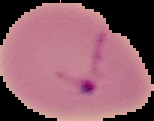
{
  "malaria_status": "parasitized",
  "preparation": "thin blood smear",
  "image_type": "segmented cell region with the area outside set to black",
  "image_size": "154×121 pixels"
}